Give the position of every leukocyte visible.
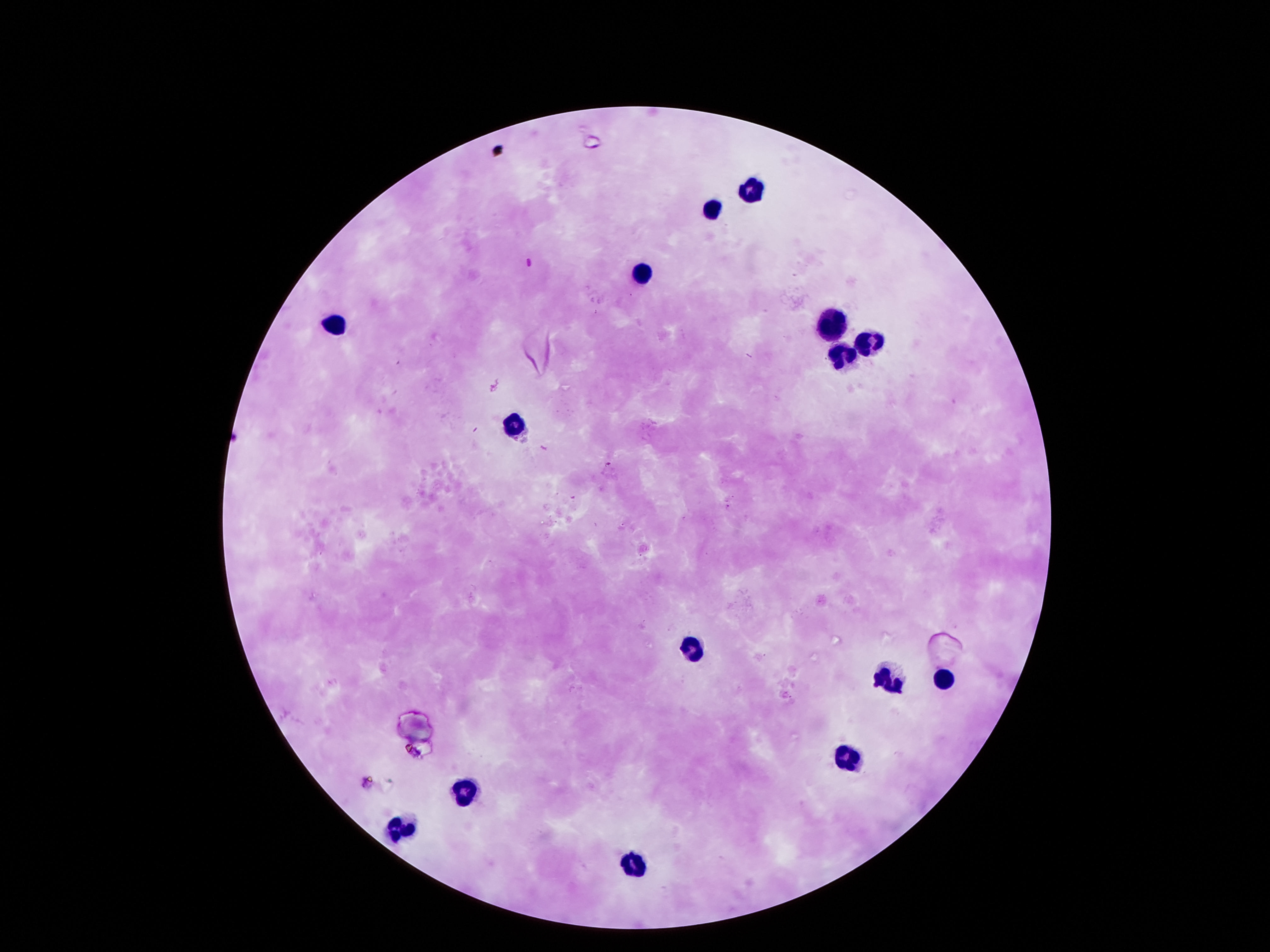

Approximate centers as [x, y] in pixels.
Leukocytes: [748, 186], [713, 206], [638, 273], [338, 323], [832, 329], [868, 339], [836, 355], [513, 423], [690, 649], [887, 674], [942, 675], [845, 756], [461, 791], [396, 827], [635, 864].

Summary:
  - Preparation: thick peripheral-blood smear
  - Patient malaria status: negative
  - Magnification: 100x
  - Field of view: single
  - Capture: smartphone camera through the microscope eyepiece
  - Image size: 1270×952 pixels
  - Stain: Giemsa